Assess for malaria.
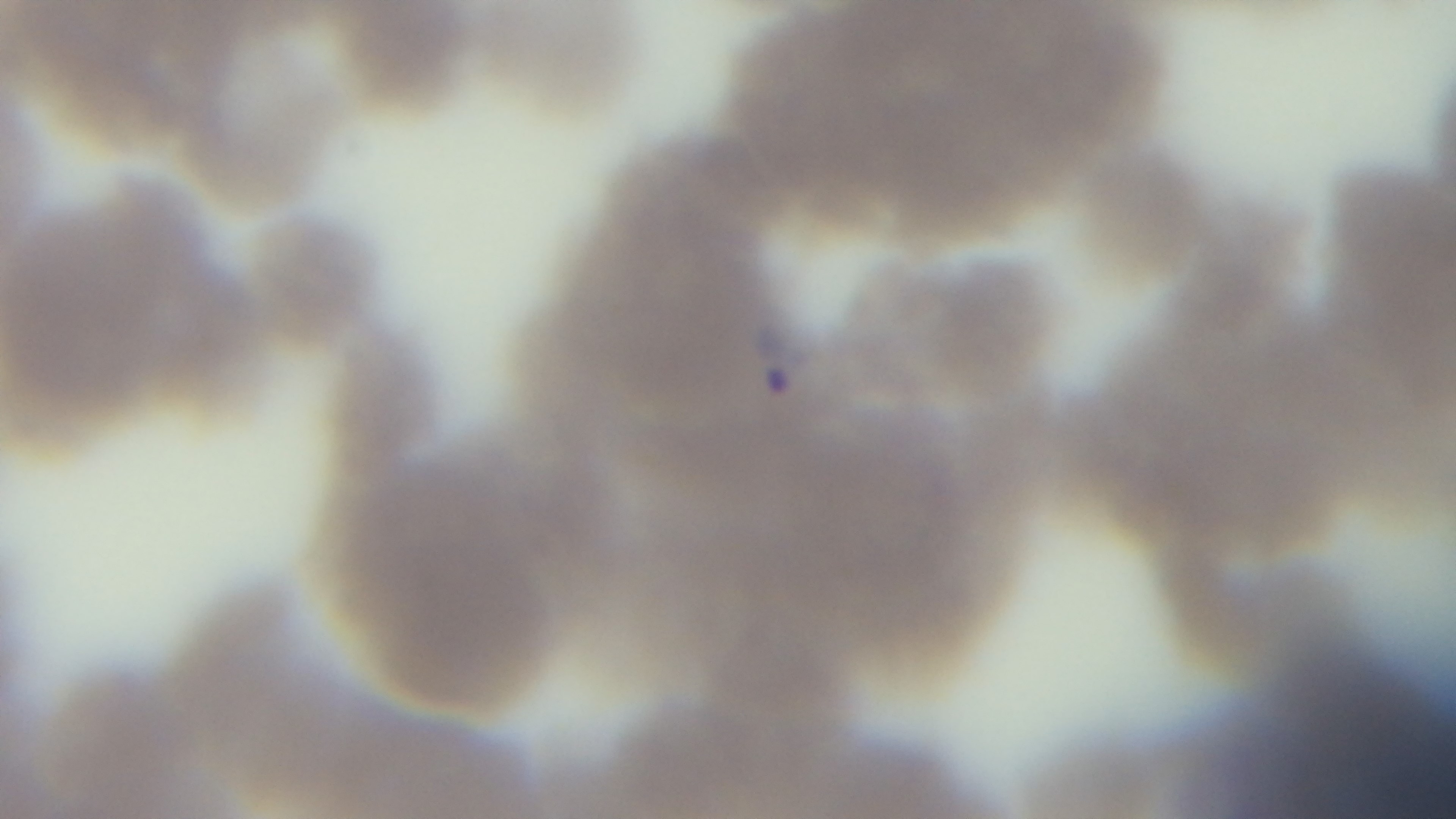

Positive.

Oil-immersion objective, 100x. Single field of view. Preparation: thin smear. Giemsa stain. Light microscopy. Captured with a mounted 4K digital camera.